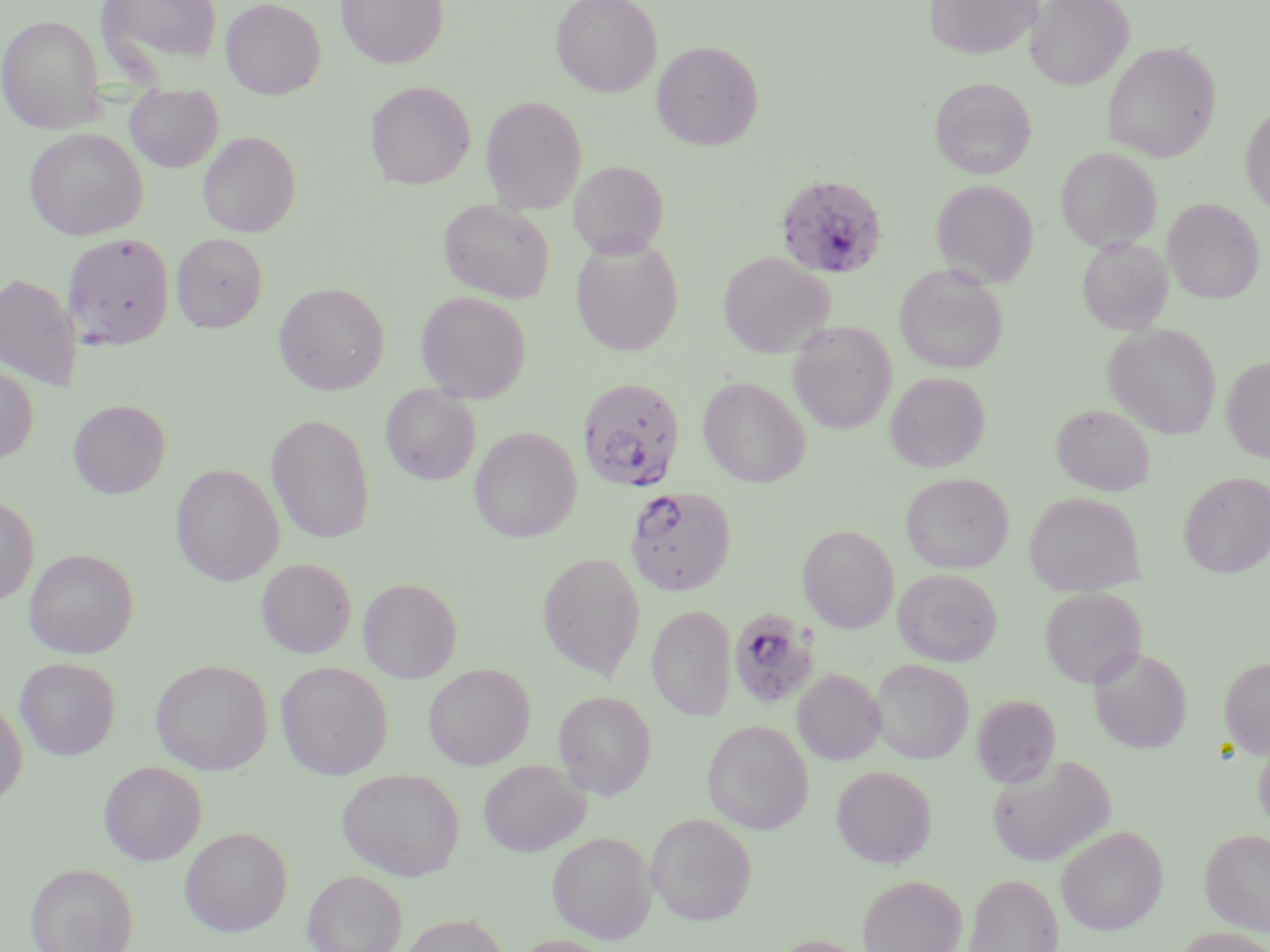
slide-level diagnosis = Plasmodium falciparum
stain = May-Grünwald-Giemsa
Plasmodium falciparum-infected red blood cell locations = approximate bounding boxes as named x1/y1/x2/y2 corners in pixels: (x1=774, y1=174, x2=889, y2=279), (x1=63, y1=232, x2=174, y2=349), (x1=578, y1=377, x2=685, y2=492), (x1=626, y1=486, x2=737, y2=595), (x1=728, y1=606, x2=821, y2=710)
magnification = 1000x
field of view = single
image size = 1270×952 pixels
preparation = thin blood smear
modality = light microscopy
uninfected red blood cell locations = approximate bounding boxes as named x1/y1/x2/y2 corners in pixels: (x1=96, y1=0, x2=224, y2=74), (x1=335, y1=0, x2=449, y2=68), (x1=551, y1=0, x2=663, y2=97), (x1=924, y1=0, x2=1042, y2=59), (x1=1025, y1=0, x2=1133, y2=90), (x1=221, y1=1, x2=325, y2=100), (x1=0, y1=14, x2=105, y2=133), (x1=652, y1=40, x2=763, y2=150), (x1=1102, y1=41, x2=1220, y2=162), (x1=930, y1=78, x2=1036, y2=179), (x1=366, y1=81, x2=475, y2=189), (x1=125, y1=86, x2=224, y2=173), (x1=365, y1=89, x2=588, y2=195), (x1=481, y1=95, x2=587, y2=214), (x1=1240, y1=104, x2=1270, y2=218), (x1=24, y1=128, x2=147, y2=241), (x1=198, y1=131, x2=300, y2=237), (x1=1055, y1=146, x2=1162, y2=252), (x1=568, y1=160, x2=669, y2=258), (x1=931, y1=180, x2=1038, y2=288), (x1=1162, y1=198, x2=1265, y2=304), (x1=438, y1=199, x2=555, y2=303), (x1=172, y1=233, x2=267, y2=332), (x1=1077, y1=236, x2=1173, y2=336), (x1=571, y1=238, x2=683, y2=357), (x1=717, y1=251, x2=834, y2=357), (x1=894, y1=266, x2=1008, y2=374), (x1=0, y1=272, x2=82, y2=391), (x1=273, y1=282, x2=390, y2=394), (x1=416, y1=291, x2=531, y2=403), (x1=788, y1=321, x2=897, y2=434), (x1=1104, y1=323, x2=1221, y2=439), (x1=1221, y1=355, x2=1270, y2=464), (x1=0, y1=364, x2=38, y2=464), (x1=885, y1=372, x2=990, y2=472), (x1=698, y1=375, x2=811, y2=488), (x1=381, y1=384, x2=481, y2=485), (x1=69, y1=399, x2=171, y2=498), (x1=1051, y1=404, x2=1155, y2=496), (x1=267, y1=414, x2=375, y2=543), (x1=469, y1=426, x2=582, y2=543), (x1=171, y1=464, x2=284, y2=586), (x1=1179, y1=471, x2=1270, y2=575), (x1=901, y1=472, x2=1014, y2=573), (x1=1025, y1=492, x2=1145, y2=595), (x1=0, y1=495, x2=39, y2=606), (x1=798, y1=525, x2=899, y2=633), (x1=24, y1=548, x2=139, y2=658), (x1=538, y1=552, x2=646, y2=680), (x1=256, y1=558, x2=356, y2=658), (x1=893, y1=568, x2=1002, y2=667), (x1=358, y1=578, x2=462, y2=683), (x1=1039, y1=587, x2=1145, y2=688), (x1=647, y1=605, x2=736, y2=720), (x1=1089, y1=647, x2=1191, y2=753), (x1=1219, y1=656, x2=1270, y2=759), (x1=15, y1=657, x2=120, y2=760), (x1=151, y1=659, x2=272, y2=774), (x1=870, y1=659, x2=973, y2=763), (x1=275, y1=661, x2=393, y2=780), (x1=423, y1=664, x2=535, y2=769), (x1=793, y1=669, x2=885, y2=765), (x1=553, y1=690, x2=656, y2=800), (x1=972, y1=693, x2=1061, y2=788), (x1=0, y1=697, x2=27, y2=808), (x1=702, y1=720, x2=813, y2=834), (x1=1254, y1=736, x2=1270, y2=831), (x1=987, y1=754, x2=1115, y2=867), (x1=479, y1=759, x2=589, y2=856), (x1=98, y1=761, x2=207, y2=865), (x1=831, y1=765, x2=937, y2=868), (x1=337, y1=768, x2=465, y2=880), (x1=646, y1=813, x2=757, y2=925), (x1=1056, y1=825, x2=1169, y2=935), (x1=179, y1=826, x2=293, y2=936), (x1=1200, y1=828, x2=1270, y2=935), (x1=547, y1=832, x2=656, y2=943), (x1=25, y1=862, x2=138, y2=952), (x1=302, y1=869, x2=408, y2=952), (x1=963, y1=873, x2=1064, y2=952), (x1=857, y1=874, x2=967, y2=952), (x1=400, y1=913, x2=507, y2=952), (x1=1171, y1=927, x2=1270, y2=952), (x1=765, y1=934, x2=874, y2=952), (x1=510, y1=935, x2=618, y2=952)